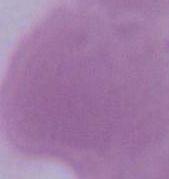

1000x magnification. A red blood cell is seen. Photomicrograph.